Give the extent of all Plasmodium falciparum-infected red blood cells.
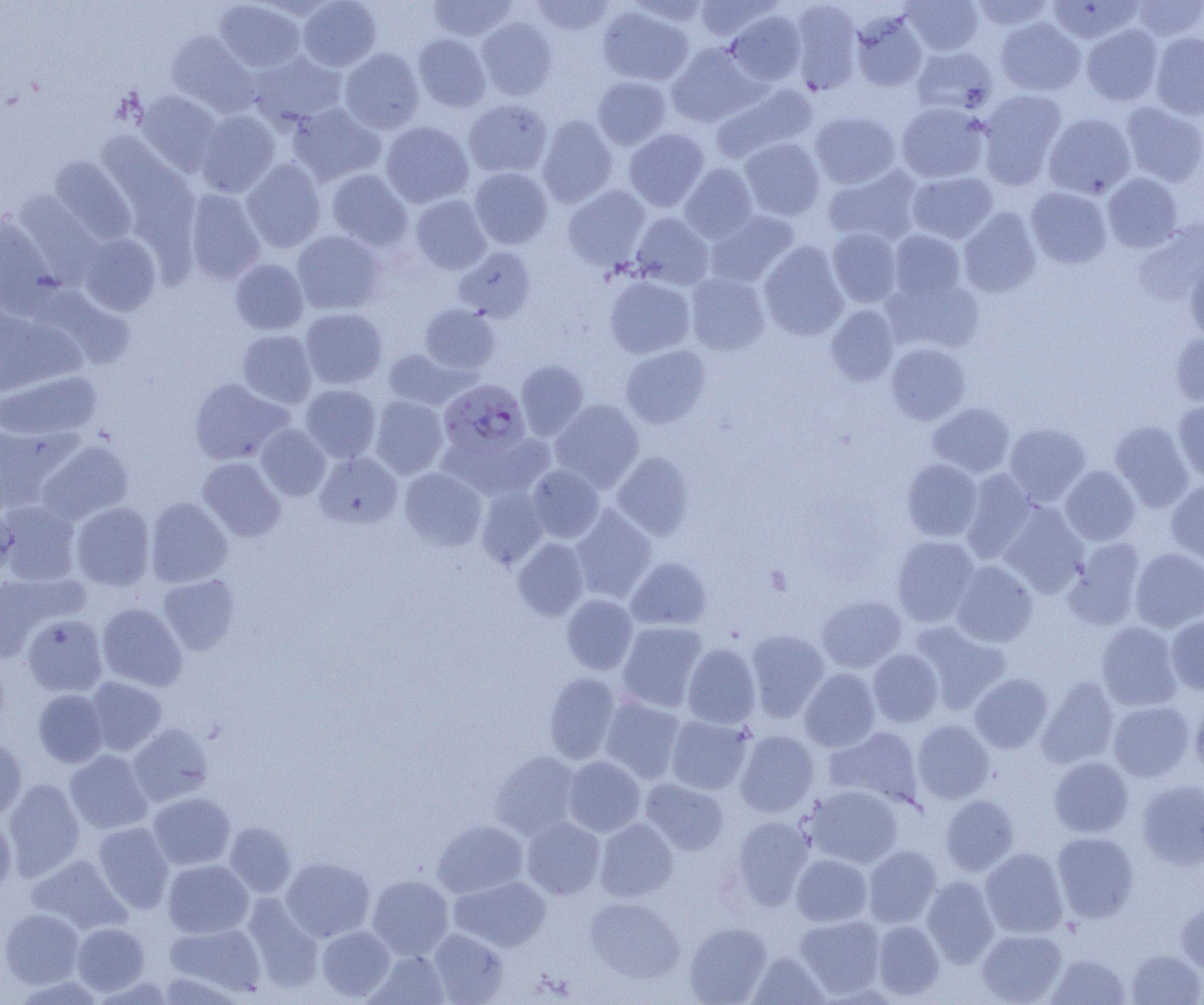
Approximate bounding boxes as (x1,y1)-(x2,y2) corner pairs in pixels.
Plasmodium falciparum-infected red blood cells: (439,379)-(530,457).

Platelet locations: (764,565)-(791,595). Uninfected red blood cell locations: (298,0)-(381,71), (428,0)-(516,41), (530,0)-(614,36), (627,0)-(710,26), (693,0)-(780,42), (902,0)-(983,55), (969,0)-(1056,33), (1128,0)-(1203,42), (214,1)-(306,73), (789,1)-(863,94), (1047,1)-(1143,43), (598,5)-(693,85), (727,10)-(807,85), (851,12)-(928,92), (477,17)-(558,100), (995,17)-(1085,95), (1081,24)-(1163,105), (166,31)-(259,117), (1150,32)-(1204,119), (413,33)-(491,112), (667,43)-(764,126), (911,46)-(998,116), (339,48)-(424,133), (248,51)-(348,129), (592,76)-(672,149), (712,83)-(817,162), (977,89)-(1067,188), (137,91)-(222,176), (464,99)-(552,178), (287,102)-(386,186), (897,102)-(990,183), (1120,102)-(1204,186), (196,109)-(280,197), (810,111)-(901,189), (1044,113)-(1136,198), (536,114)-(618,207), (381,121)-(474,207), (624,128)-(709,211), (95,132)-(194,222), (739,137)-(825,220), (48,156)-(136,243), (241,159)-(325,252), (680,162)-(758,243), (823,166)-(923,246), (470,168)-(552,249), (326,169)-(413,252), (906,172)-(998,244), (1102,172)-(1183,252), (562,185)-(650,269), (1026,187)-(1112,269), (184,189)-(266,285), (410,195)-(491,274), (959,207)-(1042,298), (704,210)-(799,288), (0,212)-(55,306), (630,212)-(714,290), (827,228)-(902,307), (291,230)-(386,315), (889,230)-(966,301), (77,233)-(162,315), (759,241)-(849,340), (454,246)-(537,322), (229,258)-(309,334), (1185,258)-(1204,345), (685,272)-(770,355), (885,273)-(985,354), (604,276)-(695,358), (419,304)-(500,374), (826,305)-(899,386), (299,308)-(387,389), (236,329)-(317,408), (1170,332)-(1204,407), (886,343)-(970,424), (620,345)-(711,428), (382,347)-(469,410), (515,360)-(589,440), (0,371)-(101,441), (189,378)-(293,465), (300,384)-(381,463), (369,395)-(449,479), (550,398)-(643,491), (1173,400)-(1204,484), (928,402)-(1015,477), (1109,421)-(1194,511), (0,422)-(68,514), (1005,422)-(1091,506), (256,423)-(331,500), (439,433)-(552,501), (36,439)-(133,524), (315,451)-(402,528), (612,451)-(694,540), (197,456)-(285,541), (902,459)-(983,541), (526,464)-(604,543), (1060,465)-(1140,545), (400,467)-(486,550), (960,470)-(1038,564), (1167,482)-(1204,566), (475,486)-(549,569), (146,496)-(232,587), (1,501)-(80,585), (70,501)-(155,591), (998,504)-(1089,597), (570,506)-(657,603), (0,507)-(17,581), (892,535)-(979,627), (512,538)-(589,621), (1064,538)-(1146,630), (1130,547)-(1204,632), (625,556)-(712,630), (951,560)-(1038,647), (0,573)-(75,662), (158,574)-(241,655), (561,594)-(638,674), (817,595)-(907,672), (97,603)-(187,691), (22,614)-(107,696), (1166,615)-(1204,694), (909,620)-(1012,713), (617,621)-(708,712), (1096,621)-(1182,710), (745,629)-(829,721), (682,643)-(761,728), (868,649)-(943,727), (800,668)-(880,752), (543,672)-(622,763), (969,673)-(1053,753), (1037,676)-(1120,767), (85,677)-(167,756), (32,689)-(108,767), (600,695)-(686,783), (1190,697)-(1204,780), (1108,701)-(1194,781), (665,715)-(753,794), (912,719)-(994,803), (126,722)-(214,807), (824,726)-(924,807), (735,729)-(818,816), (0,738)-(26,821), (64,750)-(152,834), (490,751)-(582,839), (563,756)-(645,836), (1049,756)-(1134,837), (641,778)-(729,854), (3,779)-(85,880), (1135,780)-(1204,870), (804,785)-(903,868), (147,792)-(235,870), (940,795)-(1019,876), (0,814)-(16,895), (730,815)-(814,909), (522,817)-(605,899), (594,818)-(678,901), (432,820)-(528,898), (92,822)-(174,913), (225,822)-(296,897), (1052,831)-(1139,922), (862,845)-(942,928), (980,848)-(1068,938), (791,854)-(872,926), (27,855)-(131,935), (281,857)-(375,942), (162,859)-(254,938), (367,875)-(454,960), (921,875)-(999,967), (450,876)-(551,952), (241,893)-(324,993), (585,897)-(684,983), (1176,900)-(1204,974), (1,908)-(83,989), (795,915)-(885,998), (872,920)-(945,1000), (71,922)-(150,996), (164,922)-(266,997), (684,922)-(772,1004), (316,926)-(396,1001), (428,928)-(509,1004), (977,928)-(1066,1004), (366,949)-(450,1005), (1126,949)-(1203,1005), (748,951)-(829,1004), (1046,953)-(1130,1004). Slide-level diagnosis: Plasmodium falciparum. Image is 1204×1005 pixels. Single field of view. Captured at 1000x magnification. Light microscopy. Thin blood film.